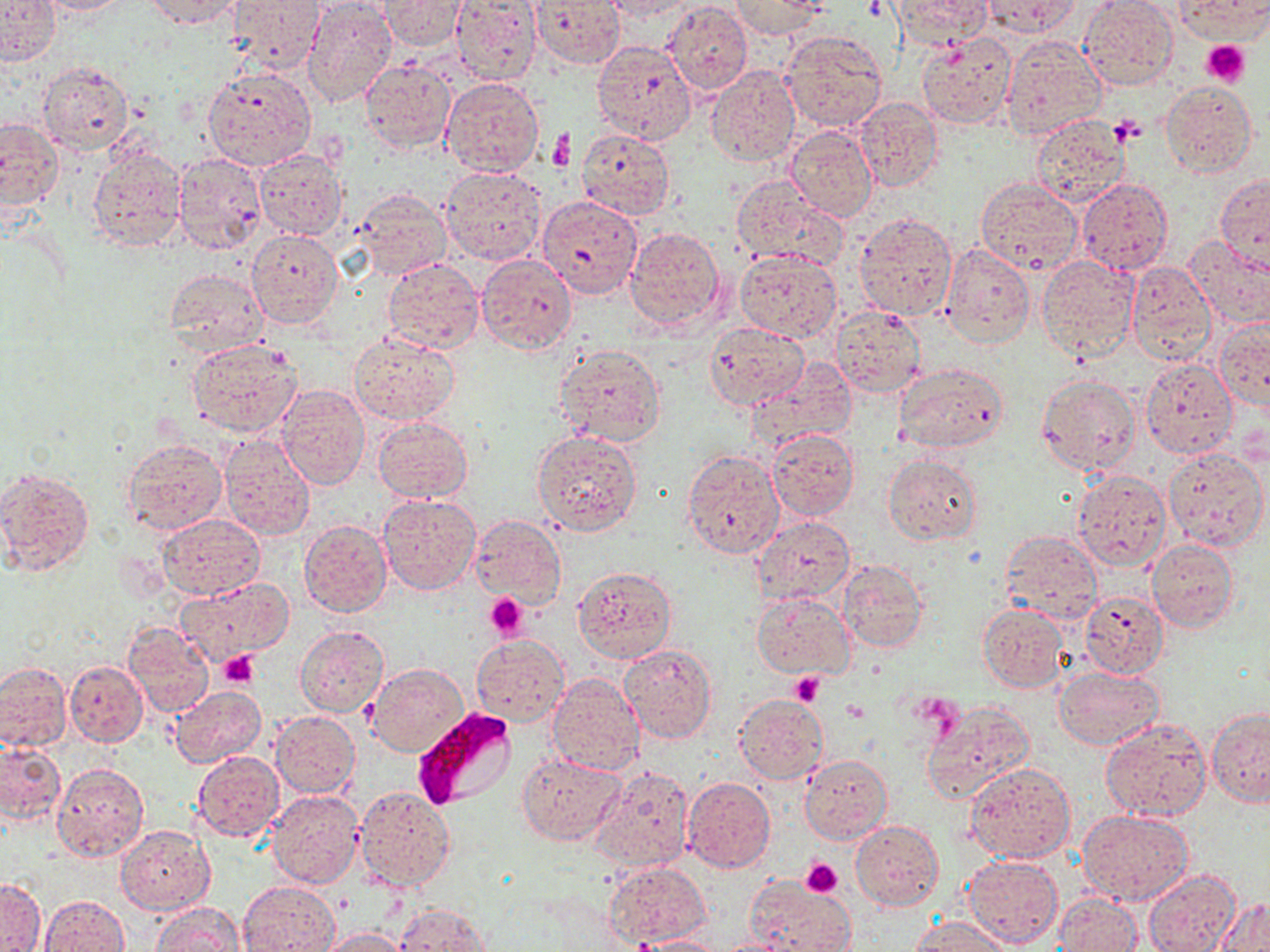

Summary:
  - Coordinate format: approximate bounding boxes as [x1, y1, x2, y2] in pixels
  - Platelet locations: [1201, 41, 1250, 87], [1109, 115, 1145, 146], [485, 593, 528, 638], [219, 651, 260, 688], [788, 671, 825, 705], [840, 700, 869, 723], [800, 858, 843, 897]
  - Plasmodium falciparum-infected red blood cell locations: [415, 708, 517, 810]
  - Uninfected red blood cell locations: [0, 0, 61, 64], [32, 0, 137, 14], [229, 0, 326, 73], [303, 0, 398, 109], [531, 0, 624, 68], [600, 0, 702, 21], [730, 0, 828, 39], [891, 0, 995, 45], [981, 0, 1083, 38], [1174, 0, 1270, 42], [142, 1, 243, 28], [381, 1, 468, 52], [449, 1, 542, 84], [1078, 2, 1177, 91], [663, 3, 753, 97], [780, 30, 889, 134], [918, 34, 1017, 130], [1001, 35, 1105, 139], [591, 39, 697, 145], [360, 58, 456, 152], [37, 62, 132, 153], [706, 66, 800, 167], [204, 68, 316, 170], [441, 77, 545, 176], [1161, 80, 1257, 175], [853, 98, 943, 194], [1030, 113, 1131, 208], [0, 118, 62, 213], [786, 125, 878, 221], [576, 129, 675, 220], [86, 147, 186, 250], [253, 149, 347, 239], [173, 153, 267, 254], [440, 165, 549, 266], [1216, 172, 1270, 271], [730, 174, 847, 272], [975, 178, 1081, 274], [1075, 178, 1173, 275], [352, 189, 451, 280], [538, 195, 645, 300], [855, 211, 957, 322], [624, 226, 727, 331], [247, 228, 343, 328], [1185, 235, 1270, 327], [940, 243, 1035, 348], [734, 251, 841, 340], [476, 254, 578, 354], [1037, 256, 1138, 362], [382, 258, 484, 353], [1124, 262, 1215, 366], [164, 269, 268, 355], [829, 305, 927, 398], [1215, 316, 1269, 410], [704, 323, 809, 412], [348, 330, 461, 424], [186, 340, 302, 438], [555, 344, 667, 446], [1140, 358, 1237, 458], [748, 359, 856, 450], [893, 362, 1008, 453], [1036, 373, 1141, 475], [278, 384, 370, 489], [372, 415, 473, 501], [766, 429, 860, 521], [532, 430, 643, 535], [219, 434, 316, 541], [121, 438, 226, 537], [1163, 448, 1269, 553], [681, 449, 784, 558], [883, 453, 982, 544], [0, 466, 95, 576], [1071, 469, 1171, 570], [377, 494, 480, 596], [752, 514, 856, 605], [158, 515, 264, 599], [470, 515, 566, 607], [299, 519, 392, 618], [998, 529, 1104, 626], [1147, 541, 1238, 632], [837, 560, 929, 655], [573, 565, 676, 663], [176, 578, 293, 665], [1080, 591, 1168, 678], [751, 592, 855, 678], [481, 597, 532, 637], [976, 602, 1069, 693], [124, 622, 214, 717], [295, 626, 389, 717], [470, 634, 568, 725], [618, 644, 717, 744], [65, 660, 148, 746], [1, 661, 72, 755], [369, 663, 468, 757], [1054, 666, 1165, 751], [546, 673, 645, 775], [170, 686, 267, 767], [733, 693, 830, 785], [921, 701, 1035, 804], [1207, 708, 1270, 807], [270, 711, 359, 798], [1100, 717, 1211, 823], [0, 739, 65, 824], [193, 751, 284, 842], [517, 751, 625, 845], [799, 753, 893, 844], [965, 762, 1075, 865], [53, 764, 149, 863], [591, 765, 694, 874], [682, 777, 775, 872], [355, 785, 455, 891], [268, 789, 363, 888], [1078, 811, 1193, 905], [851, 820, 943, 911], [116, 825, 215, 913], [962, 854, 1062, 949], [604, 862, 712, 948], [1143, 869, 1241, 952], [745, 876, 855, 952], [0, 879, 46, 952], [240, 879, 339, 952], [1054, 894, 1141, 952], [41, 895, 129, 952], [1215, 896, 1269, 950], [151, 902, 243, 951], [394, 904, 491, 951], [909, 916, 1011, 952], [319, 927, 409, 951], [632, 936, 727, 952], [710, 938, 795, 952]
  - Slide-level diagnosis: Plasmodium falciparum
  - Magnification: 1000x
  - Field of view: single
  - Stain: May-Grünwald-Giemsa
  - Image size: 1270×952 pixels
  - Modality: light microscopy
  - Preparation: thin blood film